State which parasite is depicted.
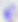
Toxoplasma gondii.

Summary:
  - Magnification: 400x
  - Modality: photomicrograph